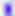

Summary:
  - Modality: micrograph
  - Magnification: 400x
  - Identification: Toxoplasma gondii